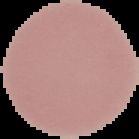

Result: no Plasmodium parasites detected. The area outside the segmented cell region is set to black. Image is 139×139 pixels. From a thin blood film.